Describe the morphology of the red blood cells.
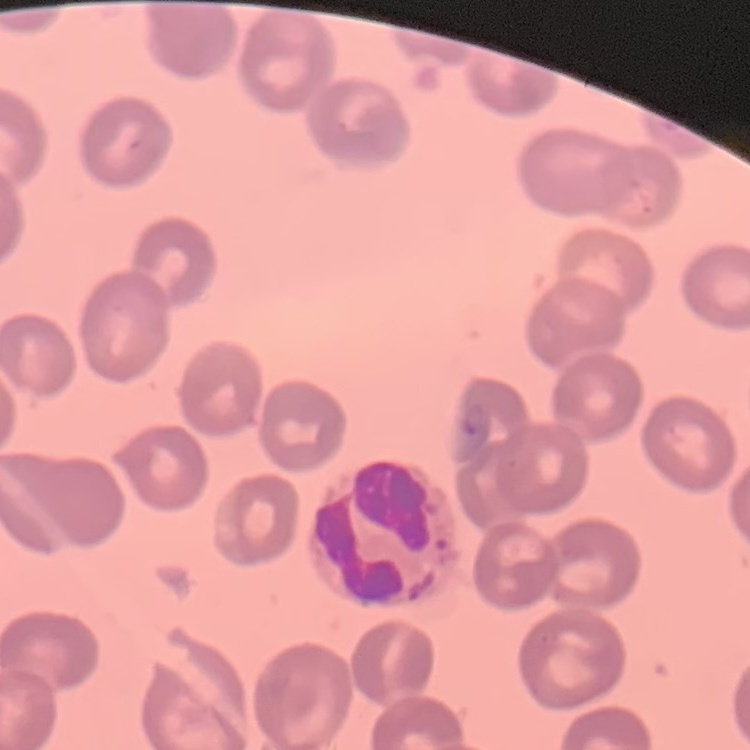

They show no rouleaux formation.

Thin blood smear. Stained with either Field's or Giemsa. Square crop of a larger photomicrograph.